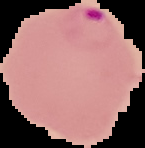
From a thin blood film. Malaria status: parasitized. The area outside the segmented cell region is set to black. Image is 145×148 pixels.